Comment on the morphology of the red blood cells.
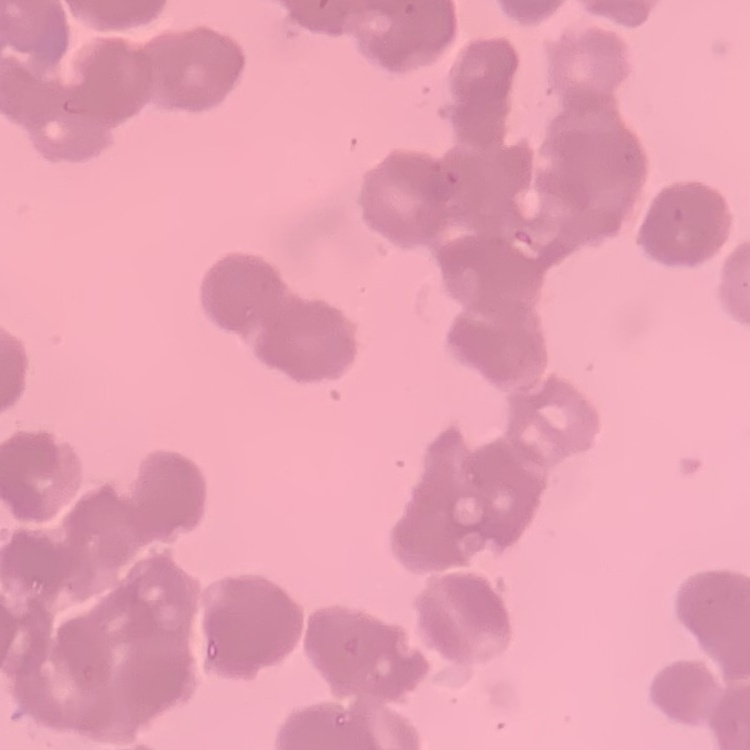

They show rouleaux formation.

{
  "stain": "Field's or Giemsa",
  "image_type": "square crop of a larger photomicrograph",
  "preparation": "thin blood smear"
}